Classify this cell by malaria status.
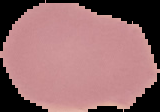
Uninfected.

Image is 160×112 pixels. Cell region segmented out of the field of view; the surrounding area is masked to black. From a thin blood smear.